Give the preparation type.
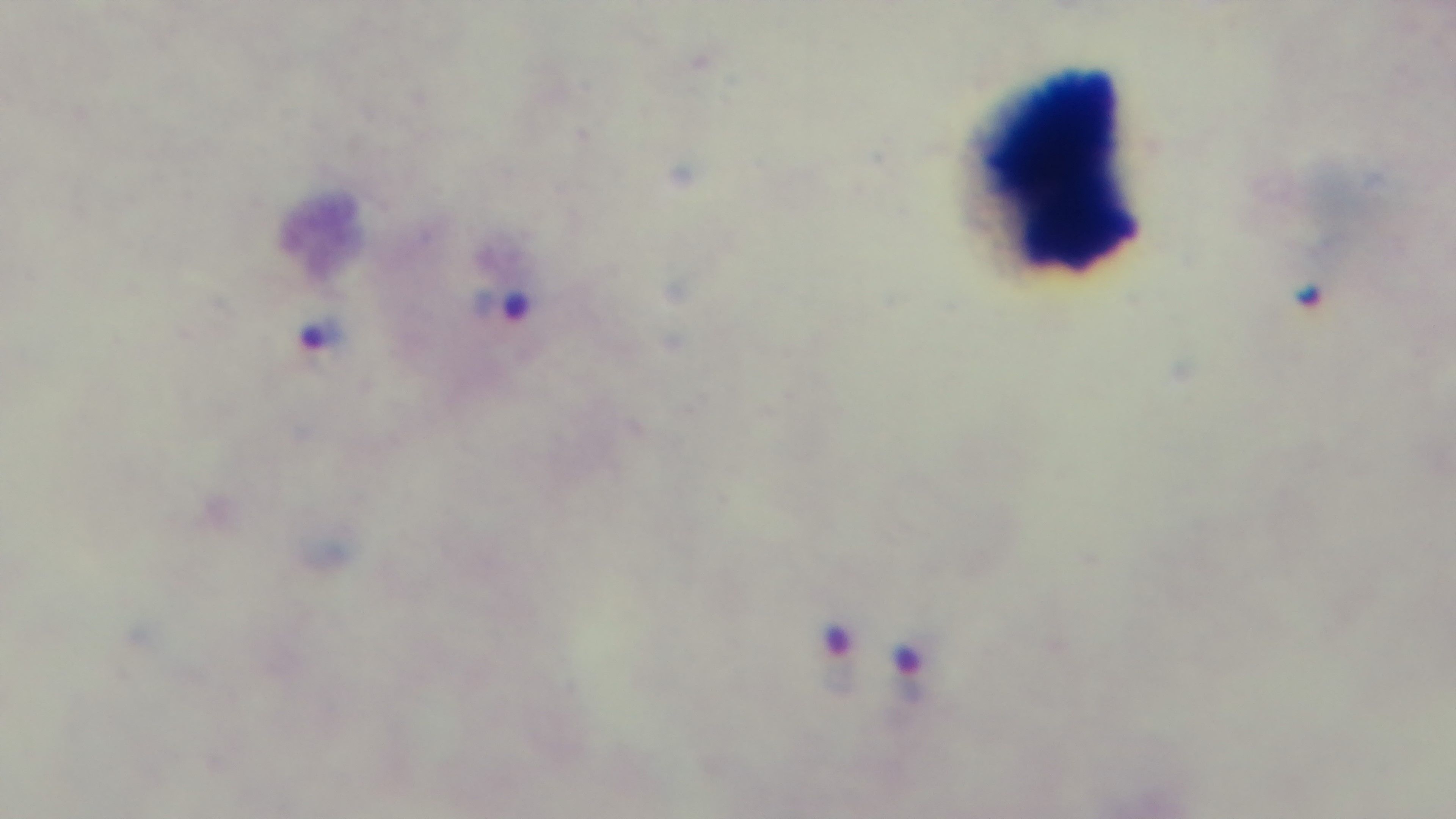
Thick.

Summary:
  - Objective: 100x oil immersion
  - Field of view: single
  - Stain: Giemsa
  - Capture: mounted 4K digital camera
  - Malaria status: infected
  - Modality: light microscopy